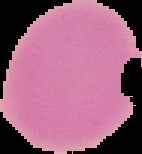

preparation = thin blood smear
malaria status = uninfected
image type = cell region segmented out of the field of view; surrounding area masked to black
image size = 142×154 pixels